Locate every uninfected red blood cell.
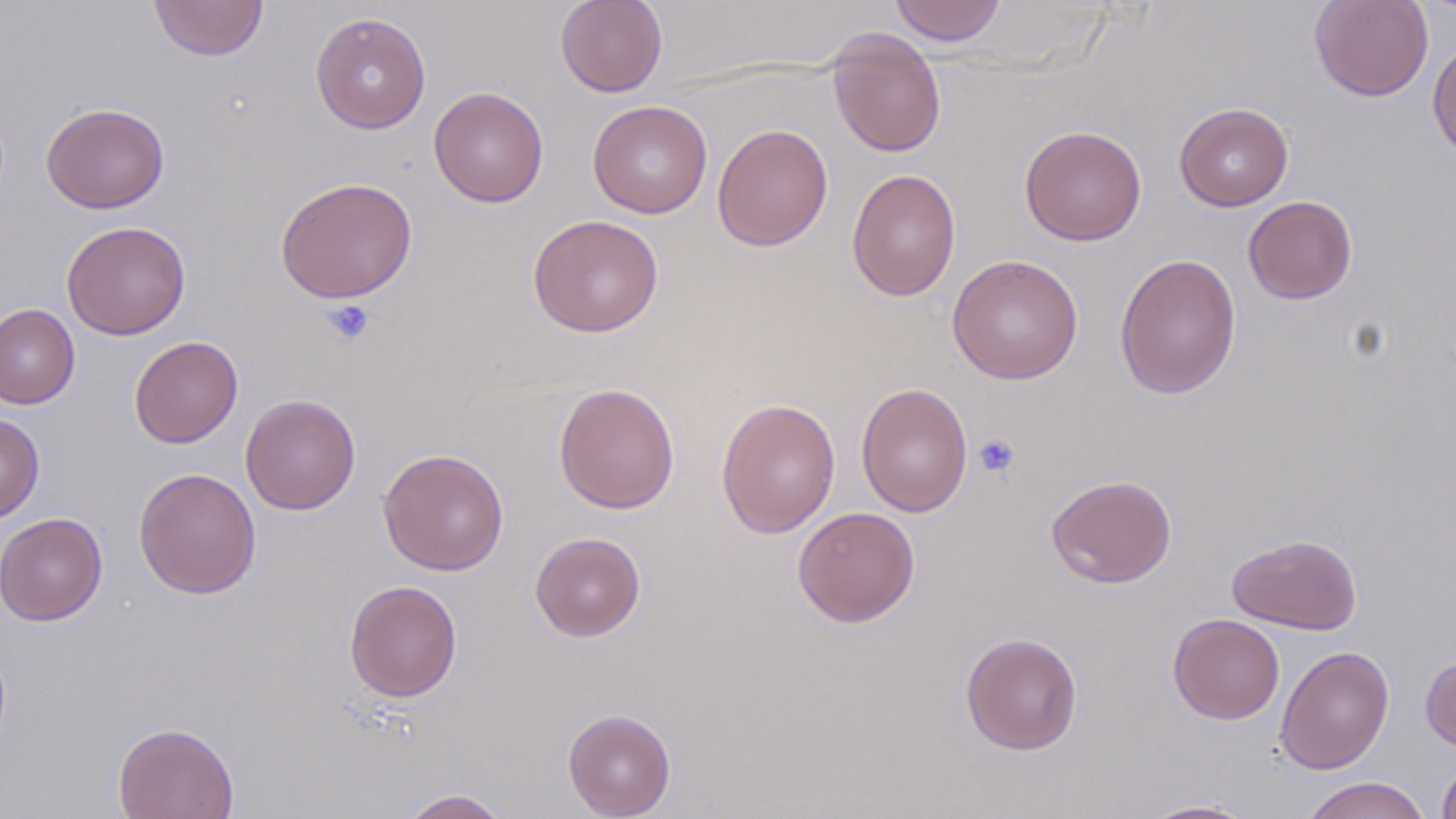

Approximate bounding boxes as named x1/y1/x2/y2 corners in pixels.
Uninfected red blood cells: (x1=149, y1=0, x2=268, y2=61), (x1=555, y1=0, x2=668, y2=97), (x1=889, y1=0, x2=1006, y2=46), (x1=1309, y1=0, x2=1434, y2=102), (x1=311, y1=11, x2=431, y2=134), (x1=826, y1=28, x2=947, y2=159), (x1=1427, y1=37, x2=1456, y2=164), (x1=428, y1=86, x2=549, y2=207), (x1=587, y1=100, x2=712, y2=219), (x1=41, y1=102, x2=169, y2=214), (x1=1174, y1=103, x2=1294, y2=211), (x1=712, y1=123, x2=833, y2=251), (x1=1019, y1=124, x2=1147, y2=246), (x1=846, y1=168, x2=960, y2=301), (x1=275, y1=176, x2=418, y2=304), (x1=1243, y1=195, x2=1357, y2=304), (x1=527, y1=214, x2=664, y2=337), (x1=61, y1=221, x2=191, y2=340), (x1=1114, y1=253, x2=1241, y2=400), (x1=947, y1=254, x2=1084, y2=384), (x1=0, y1=304, x2=80, y2=409), (x1=129, y1=336, x2=243, y2=448), (x1=553, y1=382, x2=680, y2=514), (x1=856, y1=382, x2=973, y2=518), (x1=240, y1=394, x2=361, y2=515), (x1=716, y1=397, x2=841, y2=539), (x1=0, y1=413, x2=44, y2=524), (x1=378, y1=448, x2=509, y2=575), (x1=133, y1=467, x2=262, y2=599), (x1=1046, y1=474, x2=1176, y2=588), (x1=792, y1=506, x2=920, y2=627), (x1=0, y1=511, x2=107, y2=626), (x1=530, y1=532, x2=646, y2=641), (x1=1226, y1=533, x2=1362, y2=635), (x1=344, y1=579, x2=463, y2=702), (x1=1168, y1=613, x2=1285, y2=724), (x1=960, y1=631, x2=1083, y2=755), (x1=1275, y1=645, x2=1395, y2=775), (x1=1420, y1=654, x2=1456, y2=752), (x1=562, y1=708, x2=676, y2=818), (x1=112, y1=722, x2=239, y2=819), (x1=1436, y1=753, x2=1456, y2=819), (x1=1301, y1=776, x2=1431, y2=819), (x1=399, y1=788, x2=510, y2=818), (x1=1136, y1=799, x2=1261, y2=818).

Summary:
  - Platelet locations: (x1=321, y1=299, x2=374, y2=345), (x1=973, y1=433, x2=1020, y2=479)
  - Slide-level diagnosis: negative for blood parasites
  - Stain: May-Grünwald-Giemsa
  - Preparation: thin blood smear
  - Field of view: one of a larger specimen
  - Magnification: 1000x
  - Image size: 1456×819 pixels
  - Modality: optical microscopy